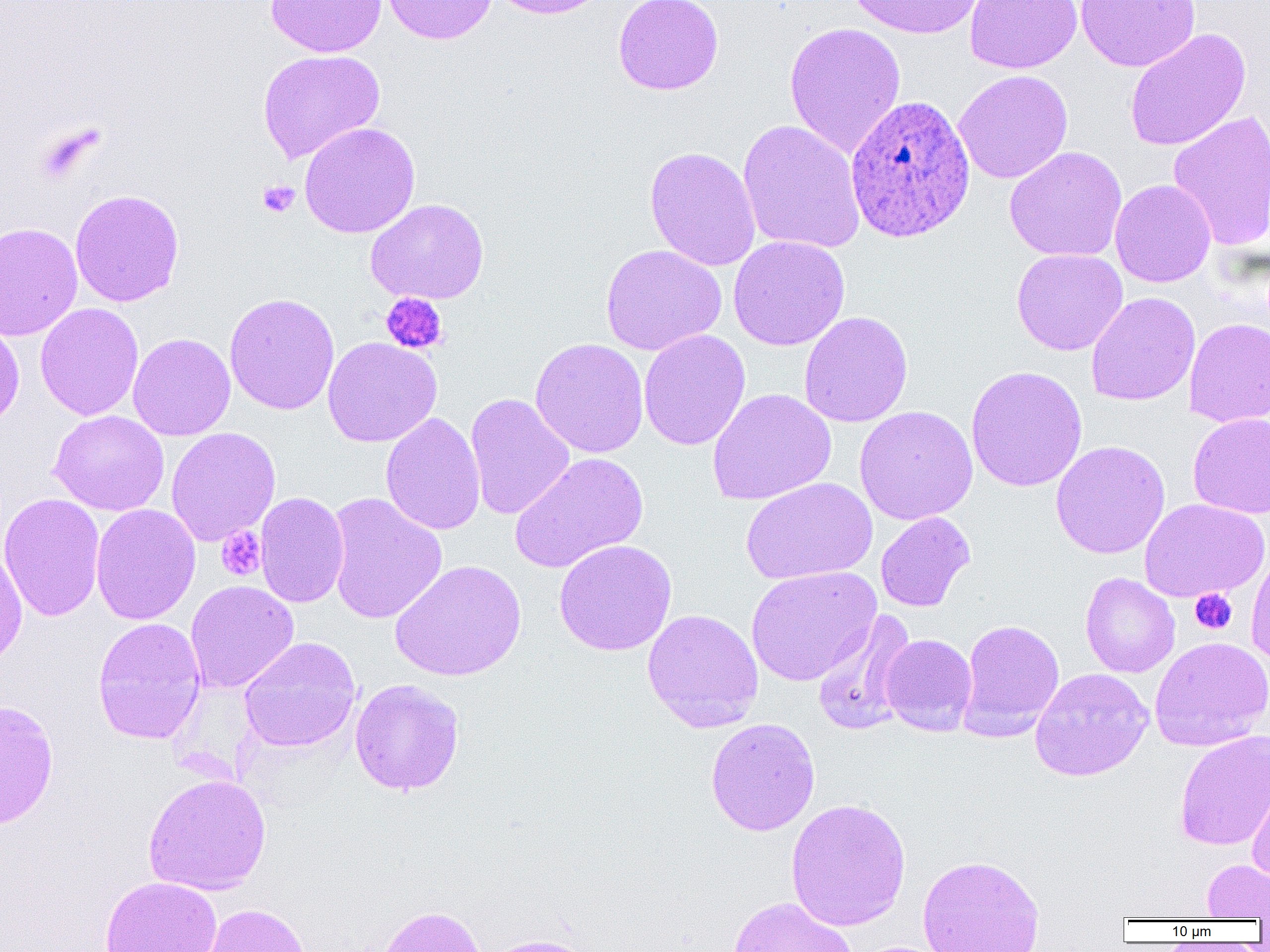
slide_level_diagnosis: Plasmodium ovale
magnification: 1000x
preparation: thin blood smear
field_of_view: one of a larger specimen
plasmodium_ovale_infected_red_blood_cell_locations: 'approximate bounding boxes as [x1, y1, x2, y2] in pixels: [844, 95, 976, 243]'
modality: light microscopy
image_size: 1270×952 pixels
uninfected_red_blood_cell_locations: 'approximate bounding boxes as [x1, y1, x2, y2] in pixels: [266, 0, 387, 58], [380, 0, 499, 44], [487, 0, 613, 19], [613, 0, 724, 95], [845, 0, 984, 39], [964, 0, 1083, 74], [1076, 0, 1201, 72], [784, 22, 906, 159], [1124, 28, 1252, 151], [257, 49, 385, 164], [953, 70, 1073, 184], [1167, 110, 1270, 253], [737, 119, 866, 254], [298, 121, 420, 239], [644, 145, 761, 271], [1004, 146, 1127, 262], [1109, 179, 1216, 288], [69, 189, 185, 307], [365, 198, 489, 304], [0, 222, 83, 341], [728, 236, 850, 351], [600, 244, 727, 355], [1011, 248, 1127, 356], [1086, 291, 1201, 407], [224, 292, 340, 415], [35, 302, 144, 421], [799, 311, 913, 428], [0, 317, 24, 432], [1183, 317, 1270, 427], [638, 329, 751, 451], [127, 332, 236, 441], [322, 337, 442, 447], [529, 337, 649, 458], [966, 365, 1088, 493], [708, 388, 837, 505], [464, 392, 575, 521], [854, 405, 978, 525], [48, 409, 169, 516], [380, 412, 486, 535], [1188, 412, 1270, 520], [166, 428, 281, 547], [1050, 440, 1170, 559], [509, 452, 649, 574], [740, 478, 877, 585], [0, 492, 105, 622], [255, 492, 350, 608], [325, 492, 447, 624], [1139, 498, 1268, 603], [90, 503, 201, 625], [875, 511, 976, 612], [554, 539, 677, 656], [0, 546, 27, 670], [1246, 548, 1270, 665], [389, 559, 527, 681], [746, 566, 881, 686], [1079, 572, 1180, 678], [184, 580, 298, 693], [642, 608, 764, 733], [811, 611, 918, 735], [92, 617, 207, 745], [958, 619, 1064, 738], [880, 634, 977, 735], [239, 637, 361, 752], [1150, 637, 1270, 751], [1030, 667, 1153, 781], [349, 679, 465, 796], [0, 698, 59, 830], [705, 717, 821, 836], [1174, 730, 1270, 851], [1246, 772, 1270, 885], [143, 773, 271, 896], [785, 797, 911, 931], [917, 854, 1045, 952], [1202, 859, 1270, 920], [100, 876, 223, 952], [727, 896, 857, 952], [201, 903, 311, 952], [374, 904, 487, 952], [479, 934, 598, 952]'
platelet_locations: 'approximate bounding boxes as [x1, y1, x2, y2] in pixels: [35, 123, 102, 183], [257, 180, 300, 218], [380, 293, 448, 355], [216, 526, 266, 581], [1190, 589, 1237, 634]'